Assess the morphology of the erythrocytes.
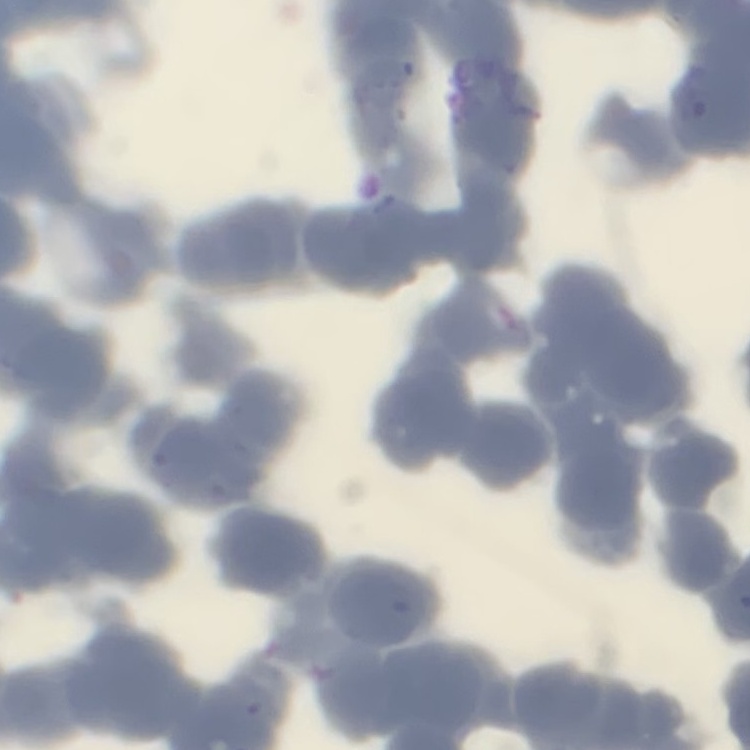
They show rouleaux formation.

Summary:
  - Image type: square crop of a larger photomicrograph
  - Preparation: thin peripheral smear
  - Stain: Field's or Giemsa